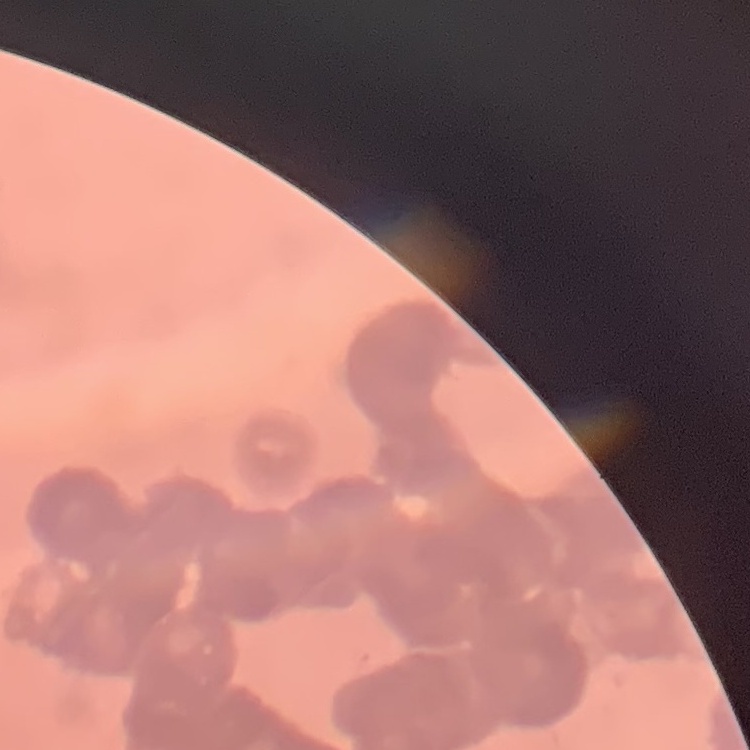
Summary:
  - Erythrocyte morphology: rouleaux formation
  - Preparation: thin blood film
  - Stain: Field's or Giemsa
  - Image type: one tile cut from a larger photomicrograph